Assess this cell for malaria.
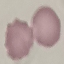
Uninfected.

stain: Giemsa
preparation: thin smear
capture: smartphone through the microscope eyepiece
image_type: automatically extracted cell patch, resized to 64 × 64 pixels